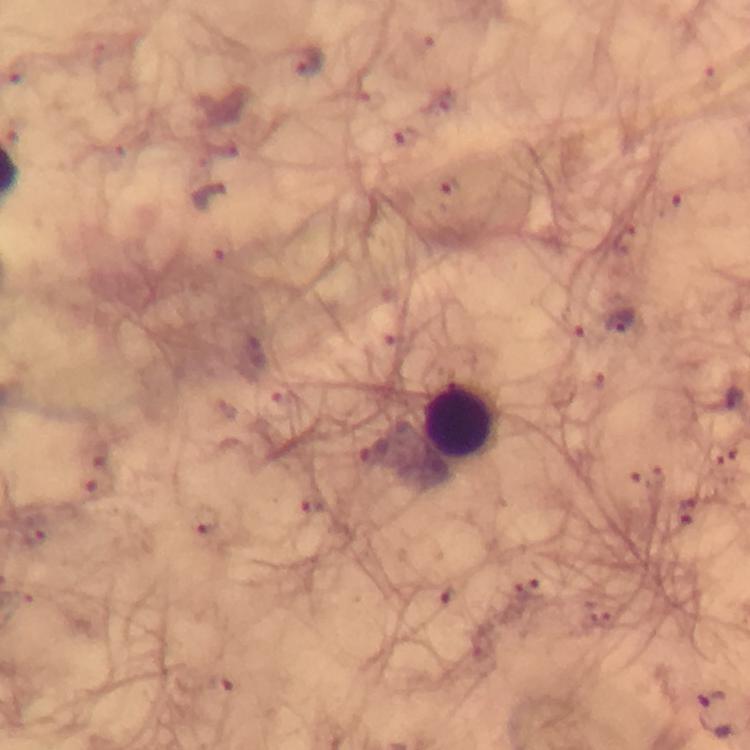

Approximate centers as {x, y} in pixels. Malaria parasite locations: {306, 62}, {406, 136}, {448, 186}, {617, 323}, {715, 715}. Leukocyte locations: {460, 423}. Thick blood smear. Immersion oil applied. A crop from one field of view. Smartphone photograph taken through a microscope. From a malaria diagnostic workup. 100x magnification. Image is 750×750 pixels. Giemsa stain.